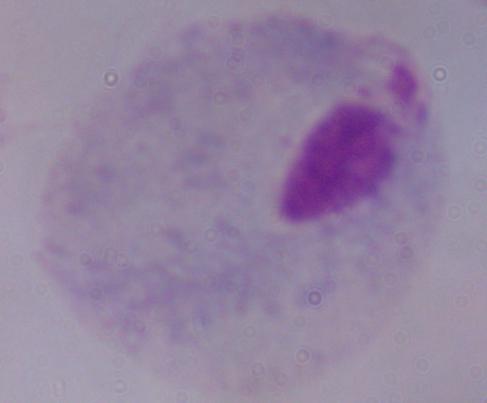 A trichomonad is seen. Micrograph. Captured at 1000x magnification.